Locate every Plasmodium parasite.
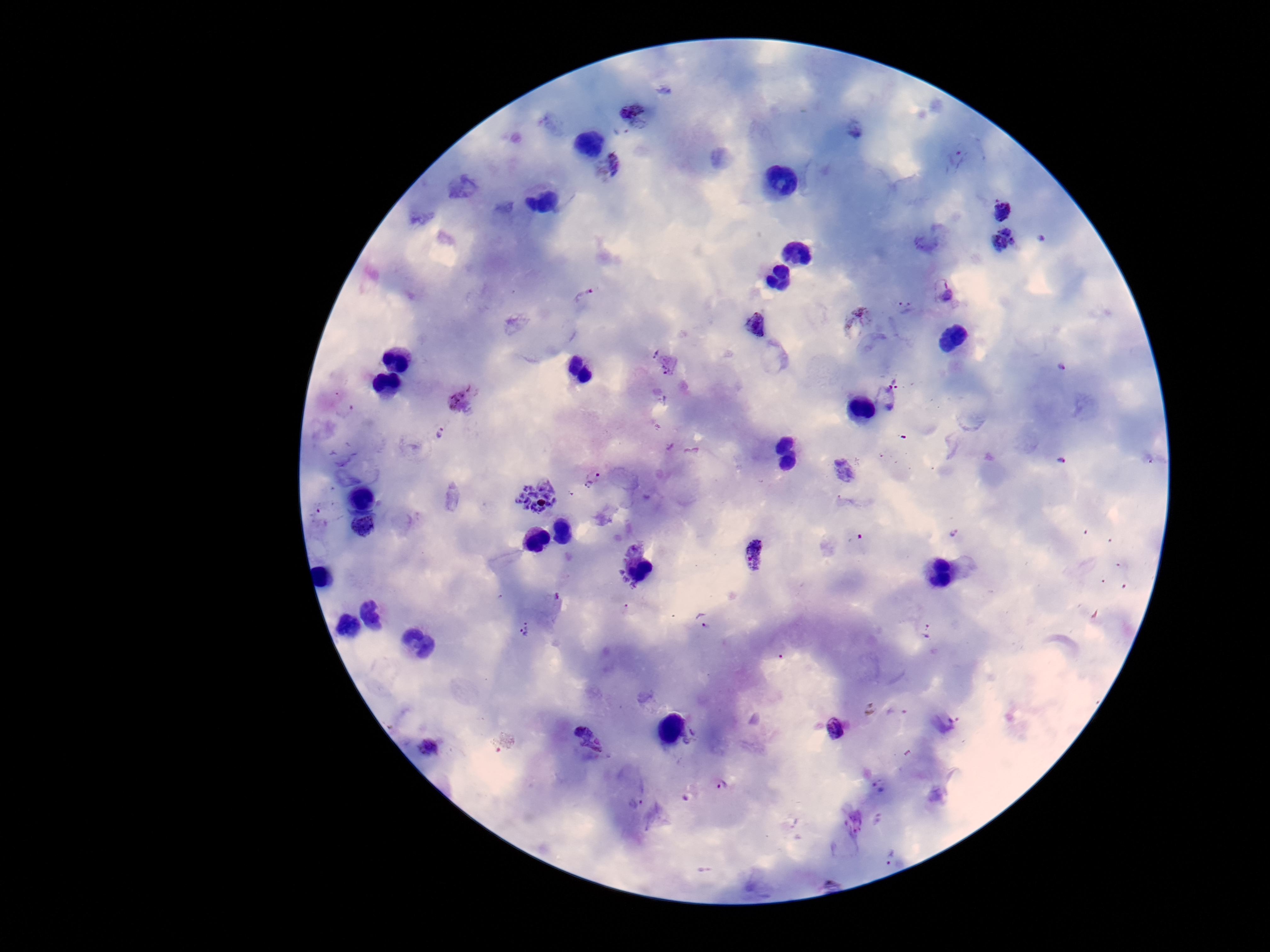

Approximate centers as {x, y} in pixels.
Plasmodium parasites: {635, 114}, {957, 160}, {606, 164}, {1002, 209}, {1043, 237}, {1006, 243}, {944, 292}, {583, 294}, {905, 308}, {855, 321}, {754, 324}, {1061, 367}, {884, 396}, {462, 399}, {343, 409}, {440, 433}, {1062, 459}, {592, 478}, {535, 496}, {364, 526}, {954, 532}, {634, 547}, {754, 555}, {619, 573}, {625, 581}, {634, 586}, {703, 620}, {526, 630}, {927, 631}, {836, 729}, {588, 738}, {690, 739}, {428, 747}, {721, 785}, {879, 786}, {636, 803}, {892, 857}.

stain = Giemsa
patient malaria status = positive
magnification = 100x
field of view = one from this slide
preparation = thick blood smear
image size = 1270×952 pixels
capture = smartphone camera through the microscope eyepiece